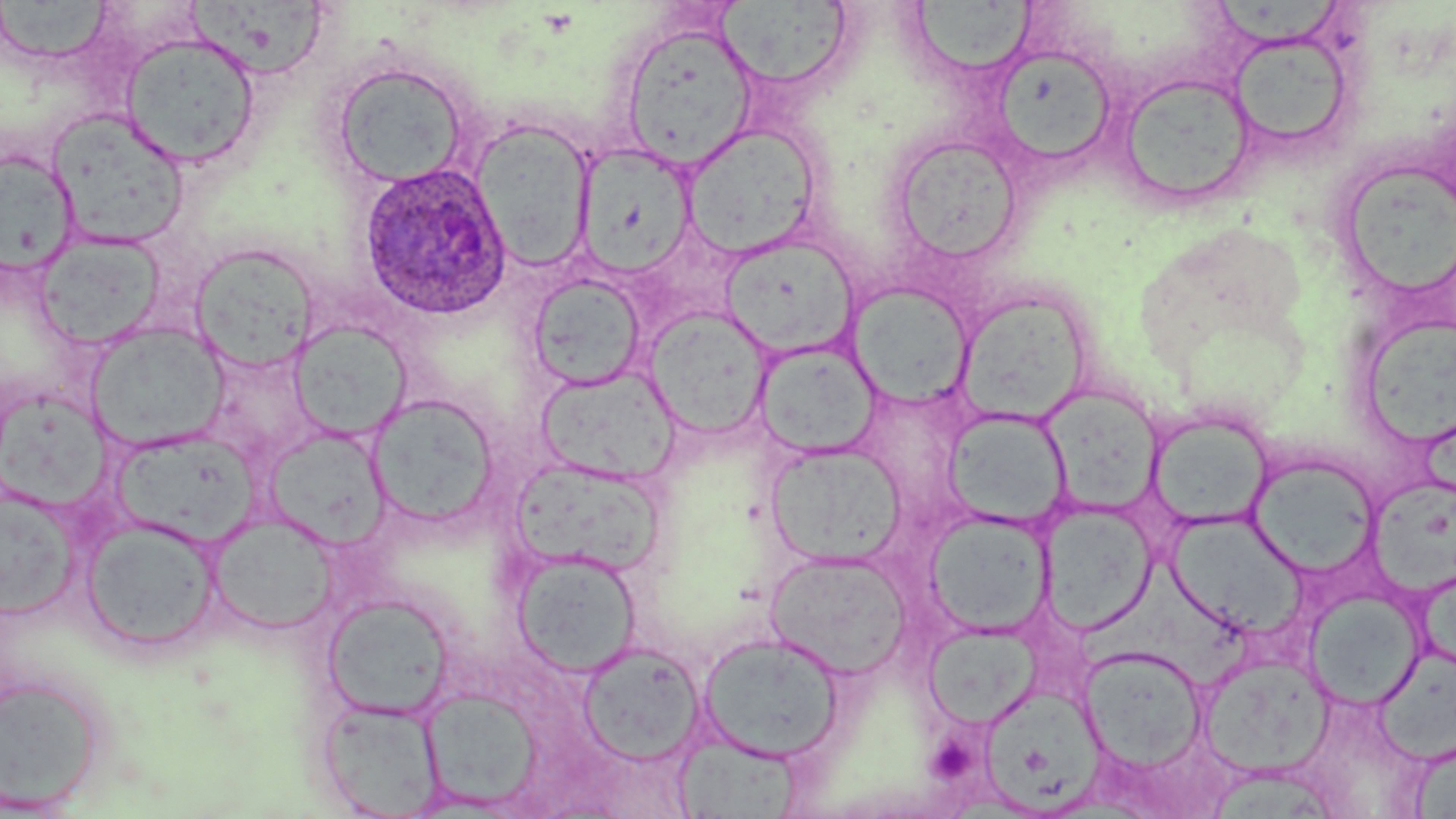

Approximate bounding boxes as (x1, y1, x2, y2) in pixels. Uninfected red blood cell locations: (180, 0, 332, 80), (1, 2, 117, 65), (617, 22, 759, 169), (1228, 29, 1357, 154), (120, 32, 260, 168), (990, 44, 1118, 169), (330, 61, 470, 188), (1117, 72, 1257, 208), (47, 108, 191, 249), (470, 118, 596, 272), (682, 123, 823, 259), (889, 135, 1024, 265), (573, 143, 698, 281), (1, 148, 79, 276), (1347, 160, 1455, 298), (34, 232, 165, 350), (720, 234, 859, 359), (189, 242, 320, 373), (527, 272, 647, 392), (848, 282, 974, 408), (956, 291, 1093, 424), (644, 306, 774, 440), (1362, 316, 1456, 451), (289, 320, 411, 440), (86, 322, 229, 452), (753, 339, 883, 460), (203, 347, 320, 465), (535, 365, 680, 485), (1041, 385, 1164, 514), (367, 394, 500, 527), (942, 409, 1071, 529), (1147, 411, 1273, 531), (263, 426, 391, 549), (112, 429, 259, 546), (765, 441, 906, 566), (1248, 453, 1380, 576), (513, 457, 666, 576), (1369, 475, 1456, 593), (0, 487, 80, 620), (1039, 503, 1157, 635), (923, 508, 1053, 638), (1166, 511, 1307, 638), (208, 512, 339, 635), (79, 516, 223, 653), (511, 548, 642, 677), (763, 549, 913, 681), (1082, 564, 1251, 683), (1304, 588, 1426, 709), (323, 593, 456, 721), (923, 622, 1041, 729), (696, 630, 846, 763), (576, 642, 705, 766), (1079, 645, 1208, 772), (1375, 647, 1456, 764), (1197, 653, 1336, 777), (0, 673, 107, 811), (983, 686, 1103, 817), (419, 687, 544, 810), (317, 698, 445, 818), (670, 733, 806, 818), (1408, 735, 1456, 818), (1208, 767, 1339, 819). Platelet locations: (933, 739, 976, 780). Plasmodium ovale-infected red blood cell locations: (357, 161, 512, 321). Slide-level diagnosis: Plasmodium ovale. May-Grünwald-Giemsa stain. Light microscopy. Thin blood smear. Image is 1456×819 pixels. Captured at 1000x magnification. Single field of view.